Outline each blood parasite and name the species.
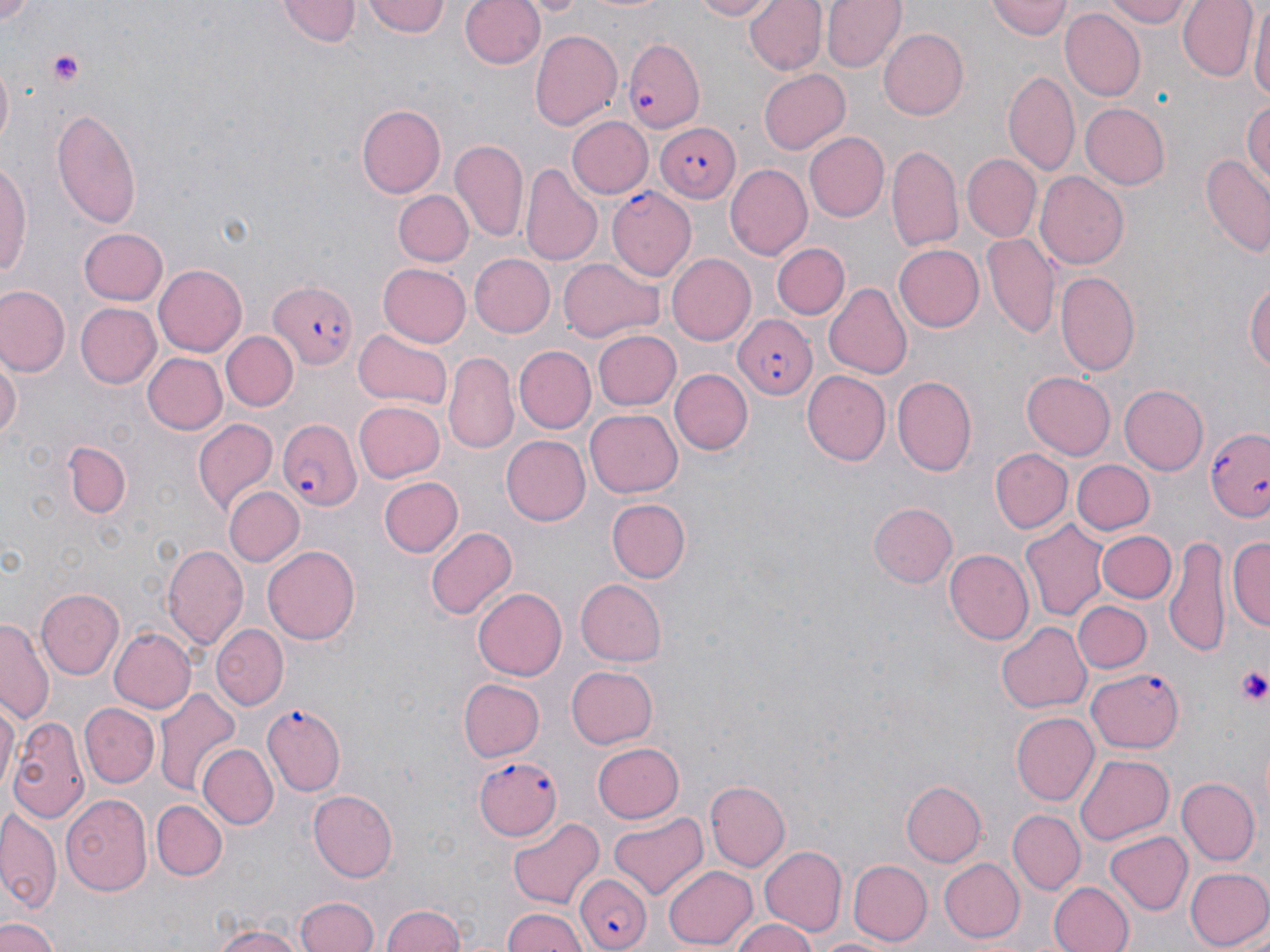
Approximate bounding boxes as (x1,y1)-(x2,y2) corner pairs in pixels.
Plasmodium falciparum-infected red blood cells: (626,38)-(706,135), (655,120)-(741,202), (609,188)-(697,280), (267,280)-(357,373), (729,315)-(816,399), (279,418)-(361,512), (1207,425)-(1270,523), (1086,668)-(1183,755), (264,702)-(346,796), (473,753)-(564,840), (573,872)-(652,951).
No Plasmodium ovale, Plasmodium malariae, Plasmodium vivax, Babesia divergens, or Trypanosoma brucei observed.

Platelet locations: (45,48)-(88,88), (1235,665)-(1270,707). Uninfected red blood cell locations: (0,0)-(35,23), (362,0)-(448,39), (458,0)-(544,71), (575,0)-(677,17), (688,0)-(782,21), (744,0)-(827,75), (823,0)-(905,72), (1102,0)-(1195,27), (1177,0)-(1255,80), (280,1)-(358,47), (985,1)-(1073,42), (1250,3)-(1269,110), (1060,9)-(1144,102), (530,26)-(622,130), (878,27)-(969,120), (758,68)-(851,153), (1003,71)-(1080,178), (1242,99)-(1270,187), (1080,102)-(1169,190), (358,103)-(446,196), (50,106)-(144,229), (566,117)-(652,199), (804,132)-(889,222), (450,139)-(528,240), (888,144)-(962,251), (965,153)-(1041,240), (1200,155)-(1270,256), (0,157)-(31,292), (523,164)-(602,268), (724,164)-(811,261), (1037,173)-(1128,269), (395,190)-(473,267), (77,228)-(168,307), (982,230)-(1058,339), (773,242)-(850,320), (895,245)-(984,332), (469,253)-(555,337), (666,254)-(755,345), (557,258)-(663,344), (377,262)-(470,347), (153,264)-(246,356), (1056,270)-(1141,379), (1247,277)-(1270,383), (823,282)-(911,379), (0,285)-(70,375), (74,302)-(161,389), (352,328)-(454,411), (594,329)-(681,411), (224,332)-(296,409), (515,345)-(595,432), (439,349)-(591,442), (0,350)-(21,444), (141,352)-(226,436), (445,352)-(517,452), (671,369)-(752,456), (803,371)-(890,465), (1022,371)-(1116,459), (891,375)-(976,476), (1120,384)-(1209,475), (354,401)-(446,483), (586,409)-(684,497), (193,417)-(278,514), (500,435)-(590,525), (67,442)-(129,521), (990,448)-(1072,533), (1074,460)-(1155,535), (378,476)-(463,557), (223,486)-(302,567), (607,499)-(690,583), (869,502)-(958,587), (1021,518)-(1108,621), (425,526)-(518,620), (1095,529)-(1176,603), (1230,533)-(1269,637), (1165,536)-(1231,657), (163,544)-(248,648), (264,544)-(360,645), (945,550)-(1034,645), (575,579)-(667,666), (37,588)-(125,679), (472,588)-(567,680), (1074,600)-(1151,673), (0,617)-(53,726), (996,620)-(1090,714), (211,624)-(287,710), (107,627)-(195,714), (564,665)-(658,749), (457,678)-(543,762), (154,690)-(242,799), (0,696)-(18,801), (79,701)-(159,785), (1010,712)-(1099,806), (9,716)-(87,824), (593,741)-(684,823), (199,744)-(278,830), (1074,753)-(1173,844), (1175,778)-(1259,866), (706,781)-(790,871), (901,781)-(986,868), (309,789)-(399,882), (62,794)-(152,895), (152,800)-(227,881), (0,810)-(61,917), (1010,810)-(1085,894), (608,812)-(709,900), (508,818)-(604,908), (1104,831)-(1192,916), (759,843)-(846,935), (937,857)-(1024,942), (849,860)-(931,944), (663,866)-(758,949), (1185,867)-(1270,950), (1049,880)-(1135,952), (296,895)-(378,952), (377,904)-(470,952), (501,908)-(591,952), (0,916)-(59,952), (728,916)-(817,952), (209,917)-(314,952), (815,933)-(901,952). Slide-level diagnosis: Plasmodium falciparum. One field of a larger specimen. May-Grünwald-Giemsa stain. Thin blood film. Image is 1270×952 pixels. Light microscopy. Captured at 1000x magnification.